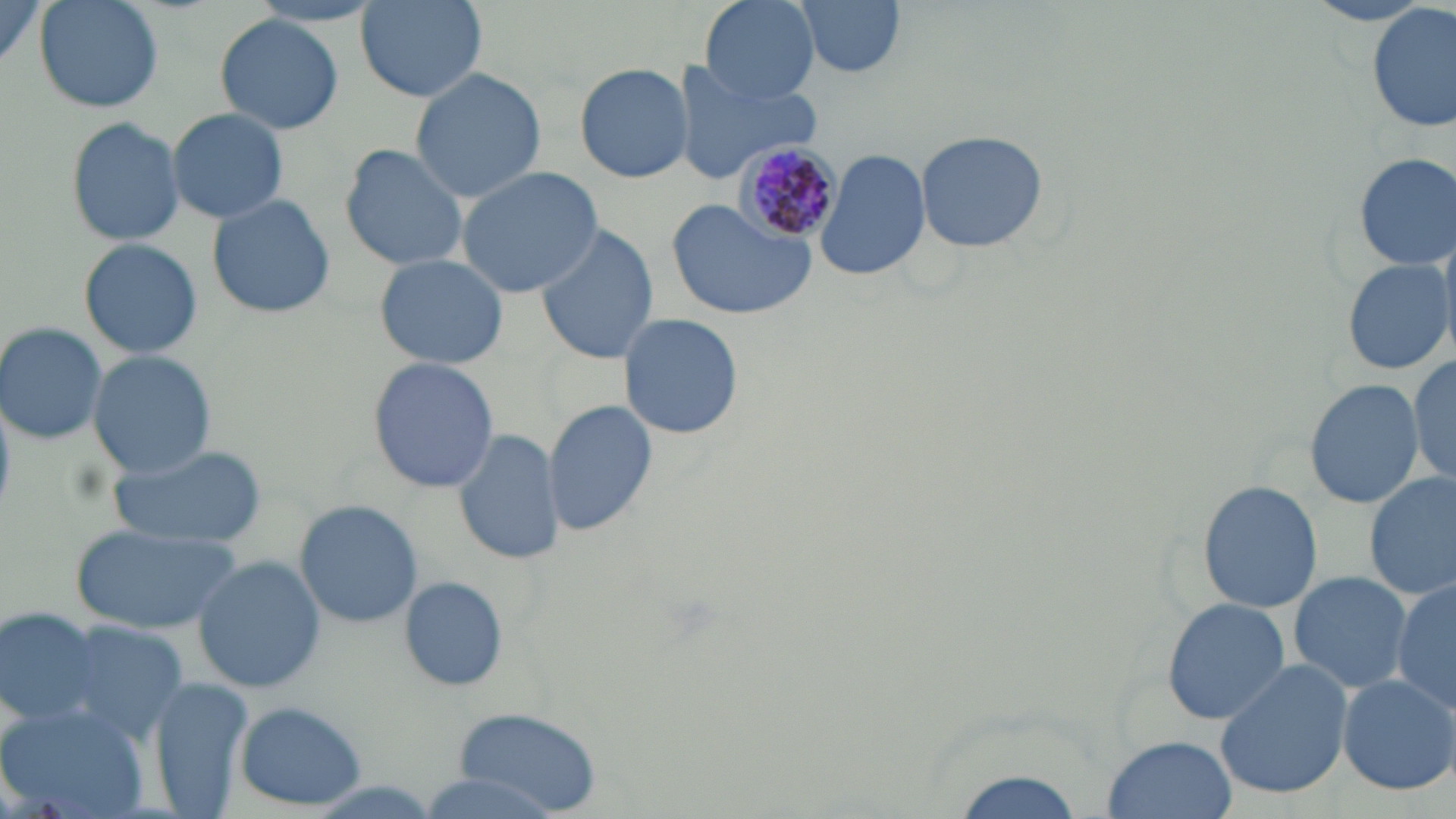
Approximate bounding boxes as (x1,y1)-(x2,y2) corner pairs in pixels. Plasmodium malariae-infected red blood cell locations: (734,139)-(844,244). Uninfected red blood cell locations: (35,0)-(164,112), (698,0)-(818,105), (792,0)-(909,79), (0,1)-(48,75), (358,1)-(485,102), (1301,2)-(1439,27), (1368,4)-(1455,133), (215,14)-(345,133), (574,61)-(694,183), (671,62)-(820,183), (407,67)-(548,203), (165,107)-(291,224), (65,116)-(186,248), (912,128)-(1051,252), (338,143)-(468,273), (815,147)-(932,284), (1349,151)-(1454,273), (455,165)-(604,298), (206,193)-(335,320), (664,201)-(815,319), (534,222)-(660,363), (77,237)-(202,360), (372,253)-(510,370), (1340,254)-(1453,378), (619,313)-(742,441), (0,322)-(109,445), (88,350)-(220,481), (1408,354)-(1456,487), (366,355)-(499,492), (1303,378)-(1425,508), (543,400)-(658,539), (452,426)-(564,567), (111,443)-(264,549), (1363,470)-(1456,603), (1197,479)-(1322,612), (293,498)-(423,630), (72,522)-(243,633), (192,556)-(326,692), (1289,570)-(1412,695), (400,578)-(508,691), (1391,581)-(1454,719), (1160,597)-(1290,724), (2,608)-(106,730), (56,620)-(191,745), (1213,660)-(1354,800), (1336,673)-(1455,795), (148,679)-(254,817), (235,701)-(369,810), (0,702)-(152,819), (451,708)-(600,816), (1102,734)-(1239,818), (942,765)-(1093,819), (419,772)-(558,817). Slide-level diagnosis: Plasmodium malariae. One field of a larger specimen. Thin blood smear. Optical microscopy. May-Grünwald-Giemsa-stained preparation. 1000x magnification. Image is 1456×819 pixels.